Report the malaria status.
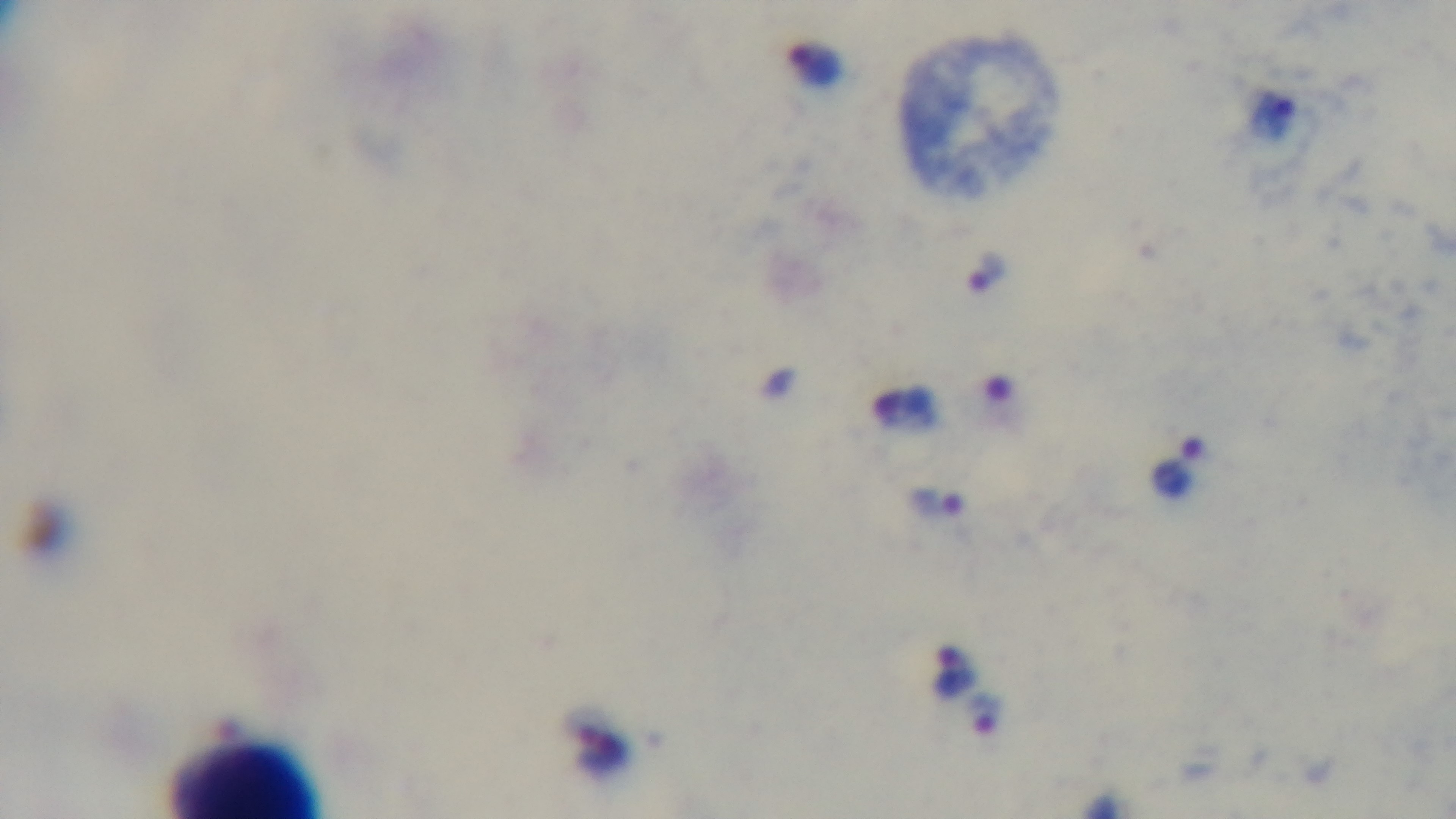
Infected.

{
  "capture": "mounted 4K digital camera",
  "modality": "light microscopy",
  "stain": "Giemsa",
  "preparation": "thick",
  "objective": "100x oil immersion",
  "field_of_view": "one from the slide"
}